Look for Plasmodium parasites.
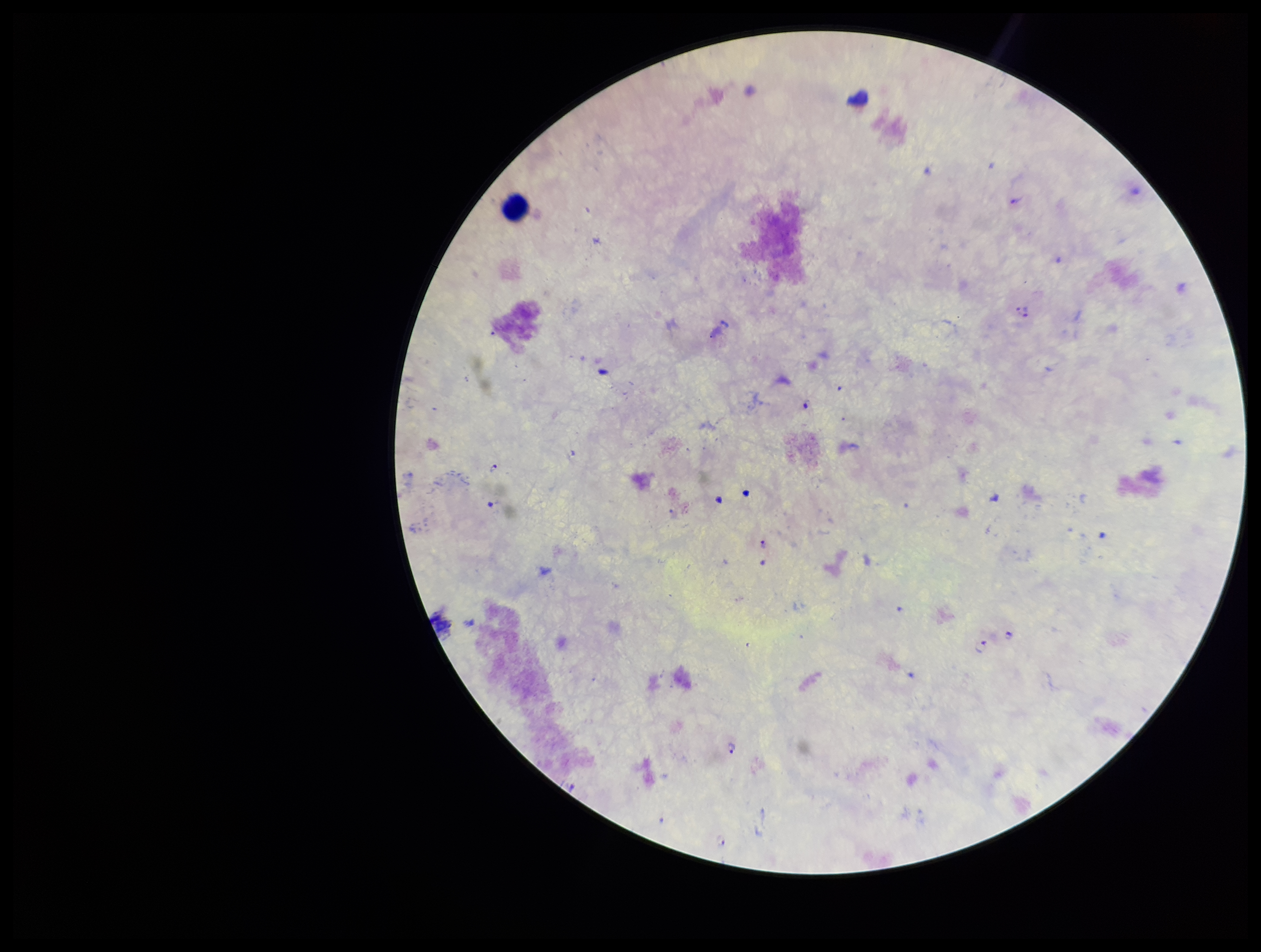

Seen.

patient_malaria_status: positive
field_of_view: single
capture: smartphone photograph through the microscope eyepiece
leukocyte_count: 1
preparation: thick smear
parasite_count: 8
stain: Giemsa
species_reported_for_this_patient: Plasmodium falciparum
image_size: 1261×952 pixels